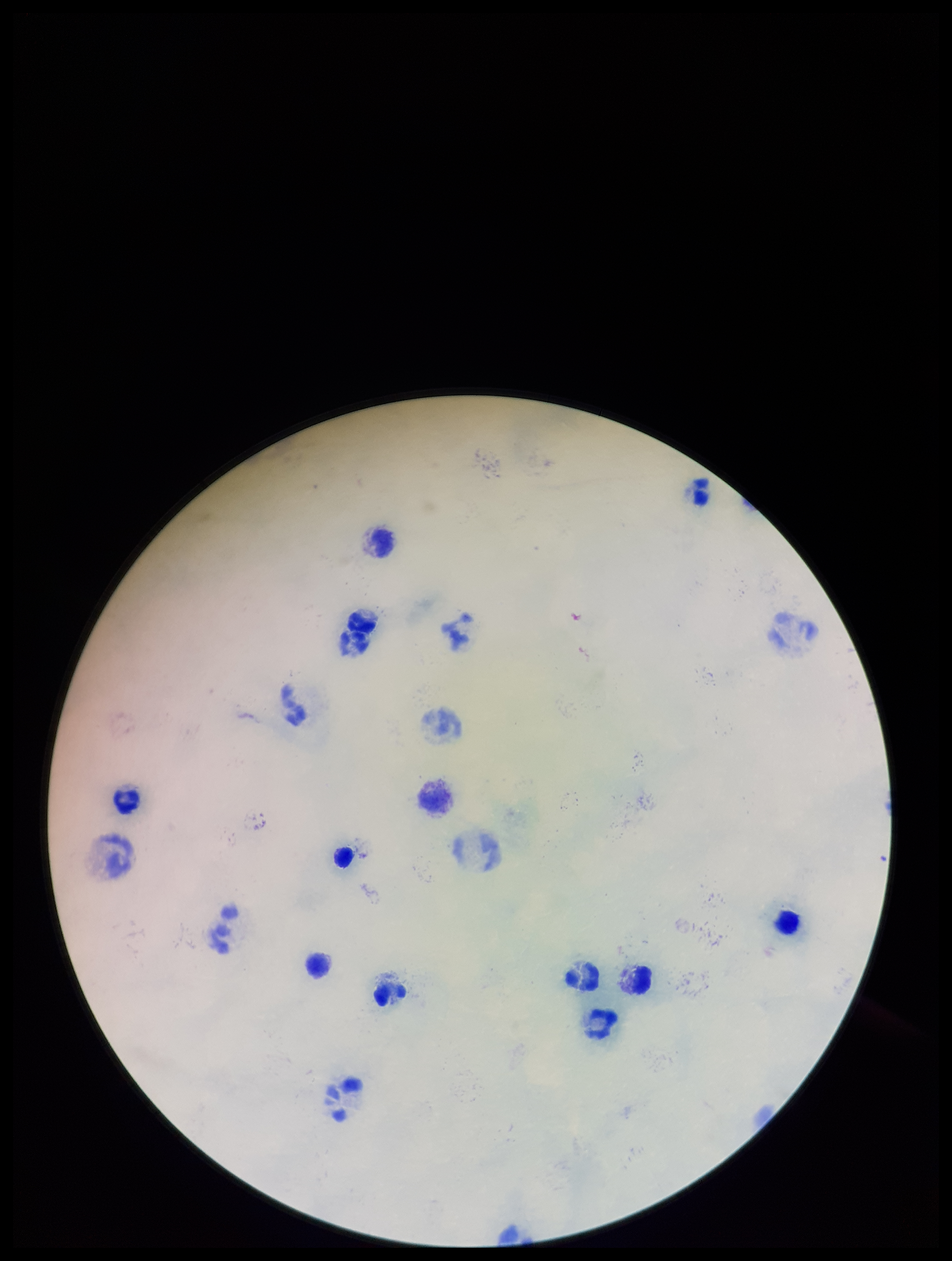
Photographed through the microscope eyepiece with a smartphone camera. Leukocyte count: 13. Parasite count: 0. Preparation: thick. Stained with Giemsa. One field from this slide. Image is 952×1261 pixels. Patient malaria status: negative. Plasmodium parasites: none detected.